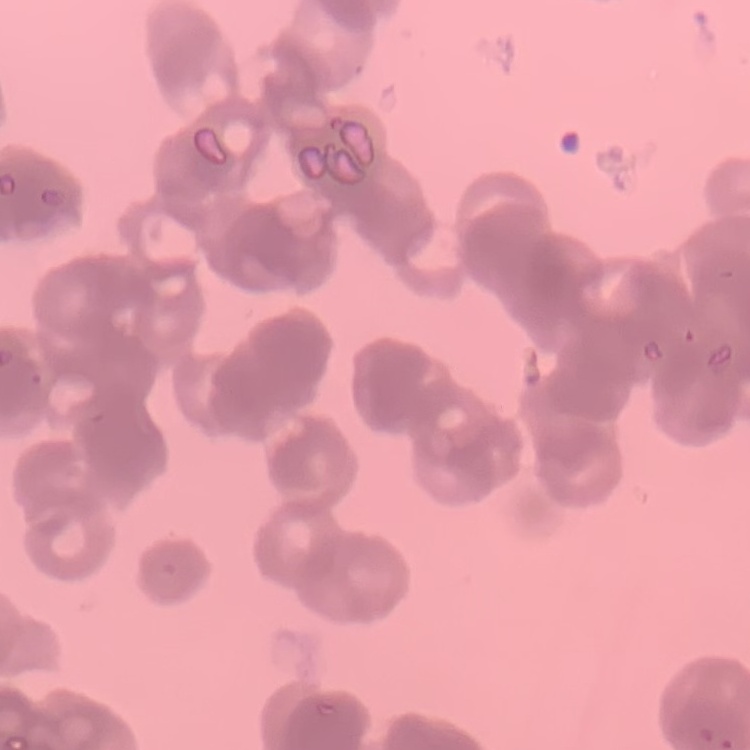
red blood cell morphology = rouleaux formation
stain = Field's or Giemsa
image type = square crop of a larger photomicrograph
preparation = thin blood smear